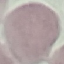
Summary:
  - Malaria status: uninfected
  - Capture: smartphone through the microscope eyepiece
  - Preparation: thin smear
  - Image type: cell patch, automatically extracted from a larger field of view and resized to 64 × 64 pixels
  - Stain: Giemsa